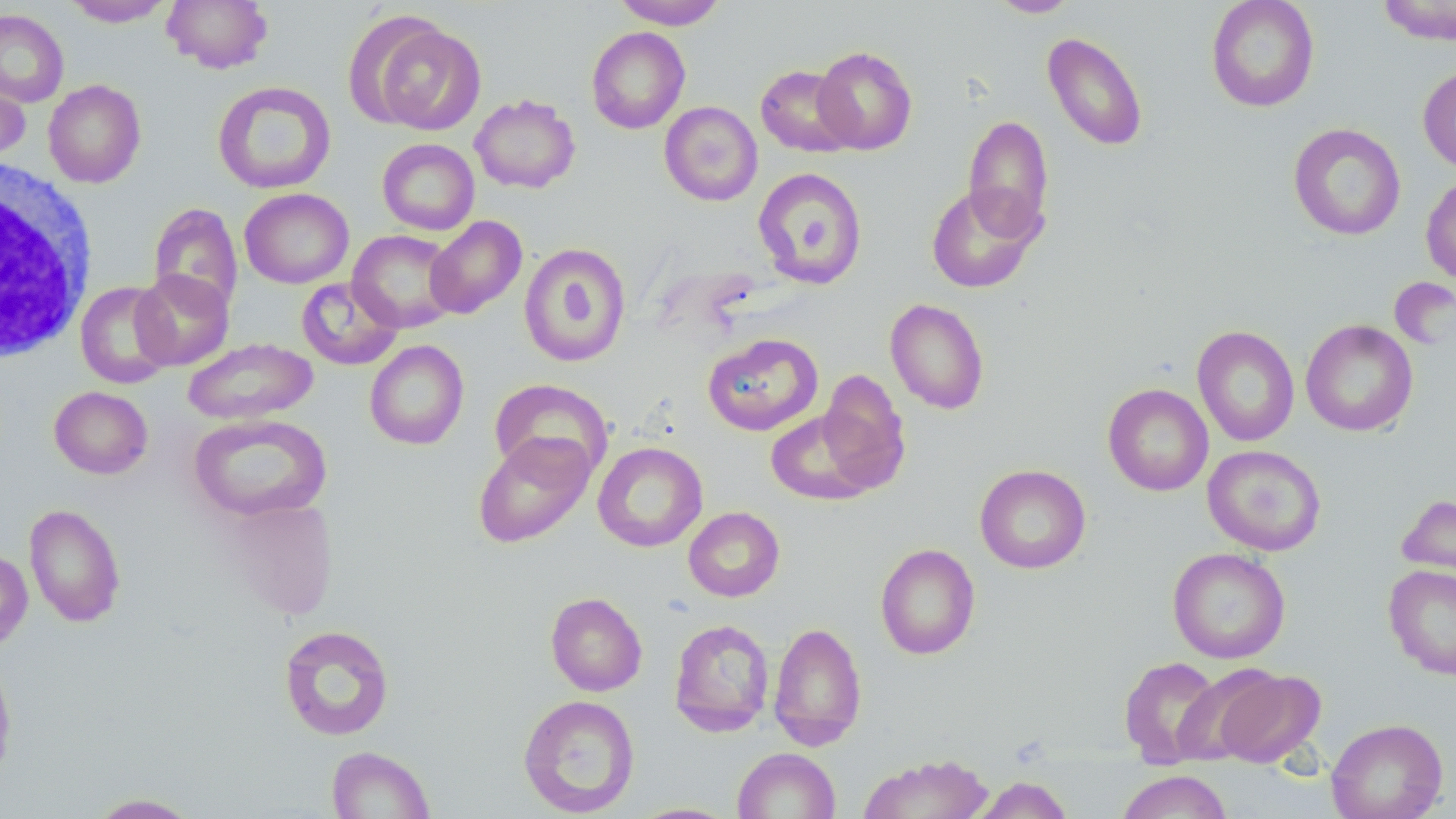

Summary:
  - Coordinate format: approximate bounding boxes as (x1, y1, x2, y2) in pixels
  - Uninfected red blood cell locations: (63, 0, 175, 27), (162, 0, 273, 73), (613, 0, 727, 30), (988, 0, 1081, 18), (1205, 0, 1321, 112), (1375, 0, 1456, 45), (0, 8, 69, 107), (363, 18, 486, 134), (586, 27, 690, 133), (1042, 31, 1149, 152), (812, 46, 918, 155), (756, 64, 859, 157), (1417, 64, 1456, 173), (0, 68, 31, 162), (43, 79, 146, 188), (212, 81, 337, 195), (470, 94, 580, 193), (659, 101, 762, 206), (963, 114, 1054, 239), (1288, 123, 1406, 241), (368, 138, 468, 330), (377, 138, 480, 236), (753, 168, 868, 288), (1420, 174, 1456, 286), (925, 182, 1045, 294), (240, 188, 354, 288), (148, 201, 243, 315), (424, 215, 527, 319), (348, 229, 461, 332), (518, 242, 631, 368), (131, 270, 234, 370), (296, 277, 403, 371), (75, 281, 176, 389), (885, 298, 989, 415), (1301, 319, 1418, 437), (1192, 325, 1300, 447), (702, 332, 823, 436), (182, 338, 318, 425), (364, 340, 469, 450), (817, 369, 911, 492), (489, 378, 614, 482), (1103, 383, 1213, 496), (49, 386, 153, 479), (765, 410, 878, 506), (187, 413, 331, 523), (472, 432, 595, 548), (592, 441, 708, 552), (1202, 444, 1326, 555), (975, 464, 1091, 574), (1397, 491, 1456, 593), (222, 497, 339, 619), (24, 504, 126, 627), (683, 506, 785, 602), (875, 543, 980, 660), (1167, 547, 1291, 664), (0, 550, 33, 651), (1383, 564, 1456, 680), (545, 591, 648, 696), (669, 618, 774, 736), (768, 621, 867, 750), (278, 624, 395, 741), (0, 656, 17, 784), (1119, 656, 1224, 766), (1210, 666, 1325, 768), (517, 694, 640, 817), (1327, 718, 1448, 819), (326, 745, 435, 818), (732, 747, 840, 819), (858, 753, 994, 818), (1116, 770, 1233, 819), (972, 775, 1074, 819), (85, 792, 202, 818), (626, 802, 743, 818)
  - White blood cell locations: (1, 159, 96, 362)
  - Slide-level diagnosis: negative for blood parasites
  - Field of view: single
  - Stain: May-Grünwald-Giemsa
  - Image size: 1456×819 pixels
  - Magnification: 1000x
  - Modality: optical microscopy
  - Preparation: thin blood smear